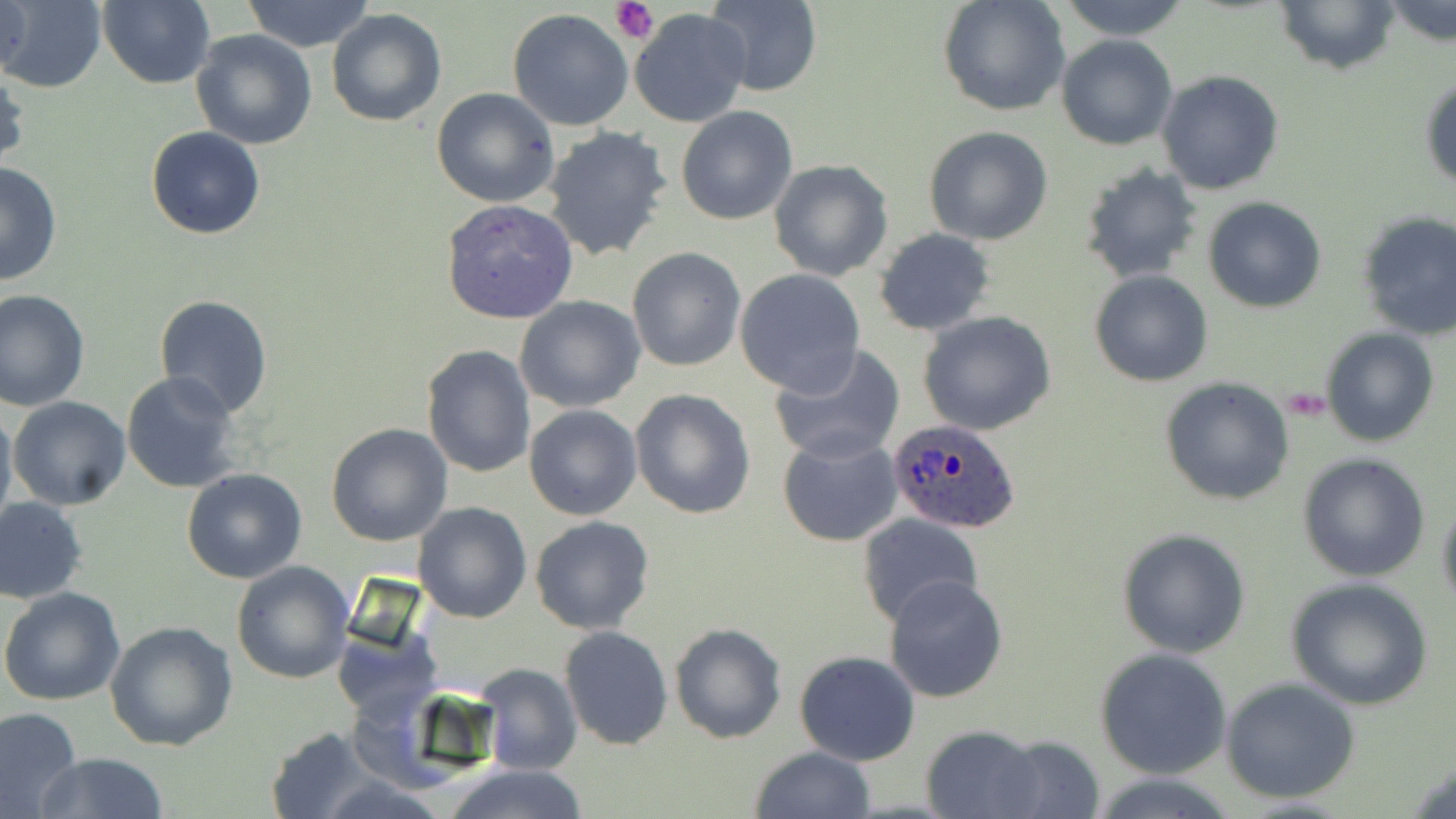 Approximate bounding boxes as (x1, y1, x2, y2) in pixels. Plasmodium ovale-infected red blood cell locations: (885, 417, 1022, 536). Platelet locations: (610, 0, 657, 45). Uninfected red blood cell locations: (2, 0, 32, 80), (98, 0, 215, 89), (242, 0, 377, 52), (703, 0, 823, 96), (937, 0, 1070, 118), (1055, 0, 1192, 39), (0, 1, 106, 91), (1275, 1, 1398, 76), (1385, 1, 1455, 49), (629, 8, 751, 127), (326, 9, 447, 128), (507, 9, 636, 131), (190, 29, 318, 149), (1057, 35, 1177, 150), (0, 64, 28, 175), (1157, 70, 1285, 195), (1420, 72, 1456, 192), (432, 86, 560, 207), (676, 105, 798, 226), (145, 126, 267, 240), (542, 126, 675, 262), (924, 126, 1054, 244), (767, 159, 894, 281), (0, 161, 62, 286), (1078, 161, 1204, 284), (439, 196, 581, 325), (1202, 196, 1326, 313), (1355, 211, 1456, 342), (873, 228, 995, 337), (626, 247, 747, 371), (734, 267, 866, 397), (1089, 270, 1214, 387), (0, 288, 90, 411), (153, 295, 274, 418), (515, 295, 646, 413), (917, 309, 1058, 437), (1320, 328, 1439, 447), (1315, 342, 1437, 551), (767, 343, 904, 465), (421, 344, 536, 480), (121, 370, 244, 494), (1158, 377, 1294, 507), (629, 388, 756, 518), (8, 396, 131, 511), (0, 399, 16, 536), (524, 404, 641, 521), (325, 423, 453, 547), (776, 432, 904, 548), (1296, 452, 1430, 582), (181, 468, 308, 584), (1436, 495, 1456, 613), (0, 497, 87, 603), (413, 501, 531, 622), (857, 513, 983, 631), (530, 517, 655, 635), (1116, 528, 1250, 658), (231, 560, 354, 683), (882, 573, 1009, 703), (1285, 577, 1434, 709), (1, 588, 127, 707), (106, 622, 238, 752), (668, 623, 788, 744), (559, 625, 672, 751), (1095, 647, 1233, 779), (794, 652, 920, 766), (476, 664, 582, 776), (1221, 677, 1360, 804), (0, 706, 82, 818), (919, 723, 1048, 819), (262, 727, 383, 817), (992, 734, 1105, 817), (750, 746, 875, 819), (34, 754, 171, 818), (440, 762, 589, 819). Slide-level diagnosis: Plasmodium ovale. Thin blood film. May-Grünwald-Giemsa-stained preparation. Single field of view. Light microscopy. Captured at 1000x magnification. Image is 1456×819 pixels.